Assess this cell for malaria.
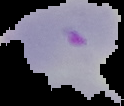
It is parasitized.

image_size: 124×106 pixels
image_type: segmented cell region with the area outside set to black
preparation: thin blood film